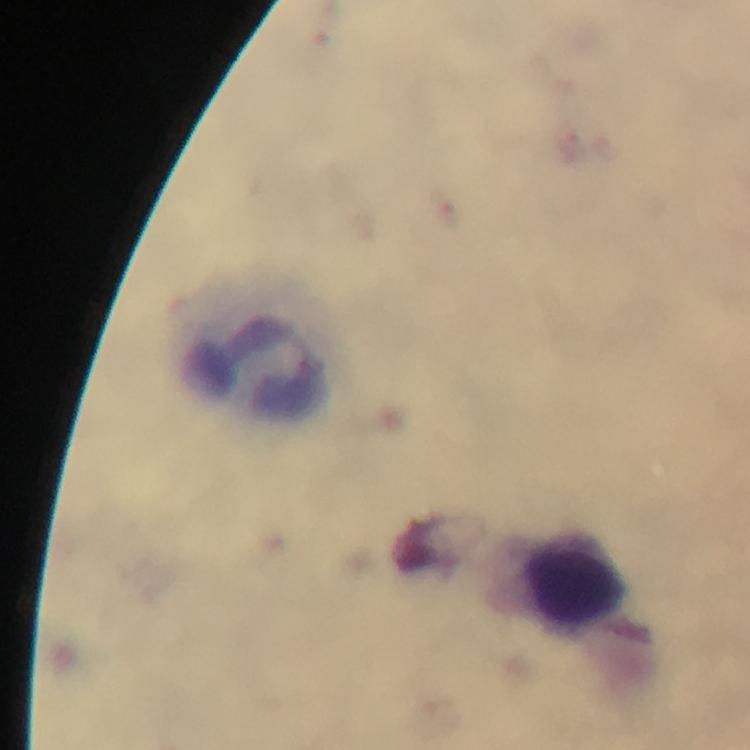 Approximate centers as {x, y} in pixels. Leukocyte locations: {258, 349}, {561, 586}. Plasmodium parasites: none detected. Thick blood smear. From a malaria diagnostic workup. Immersion oil was used. Smartphone photograph taken through a microscope. Image is 750×750 pixels. Giemsa stain. A crop from one field of view. 100x magnification.